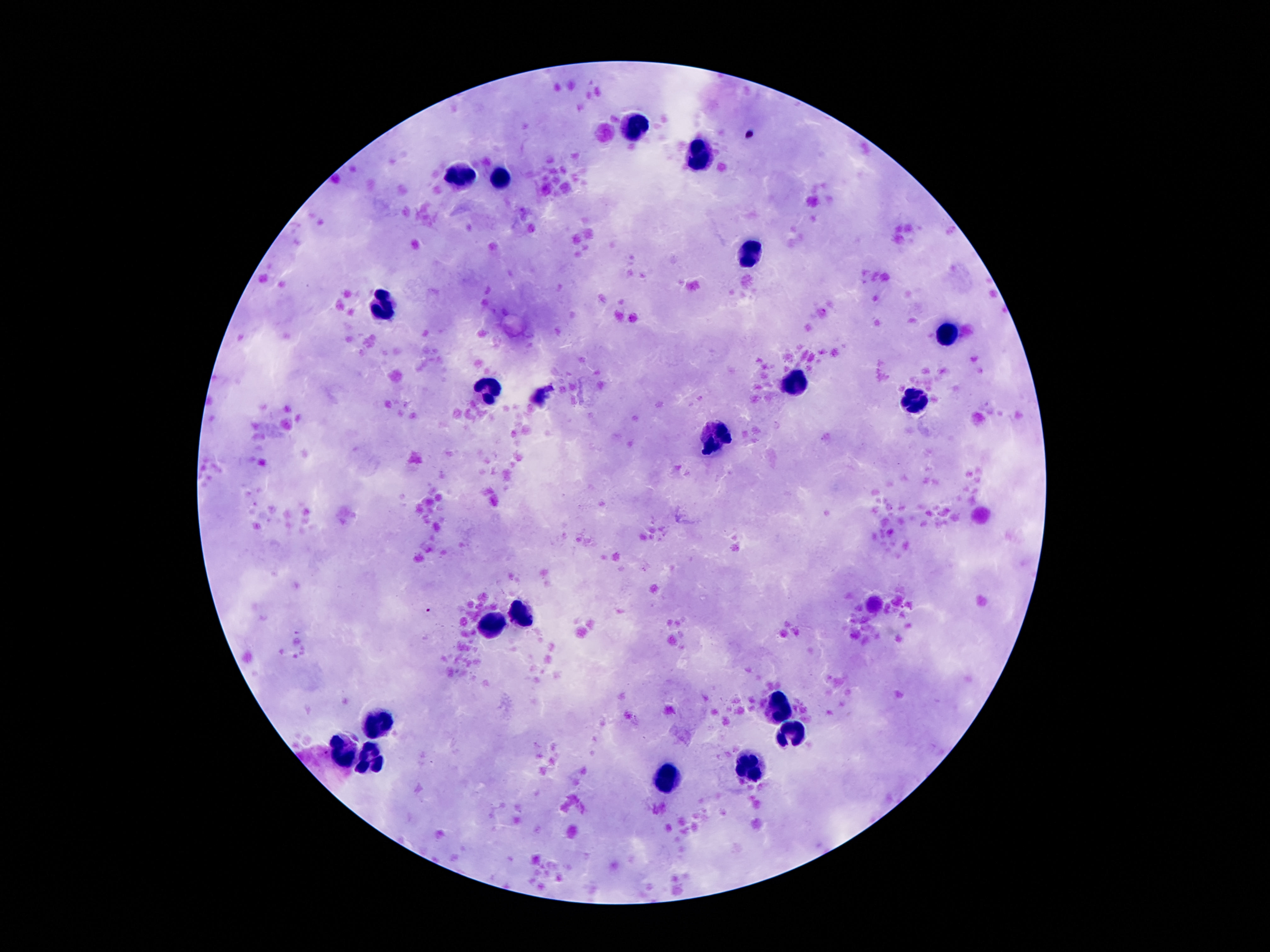
field of view = single
patient malaria status = negative
magnification = 100x
image size = 1270×952 pixels
capture = smartphone camera through the microscope eyepiece
preparation = thick blood smear
leukocyte locations = approximate object centers, in pixels from the top-left corner: (x=634, y=130), (x=701, y=158), (x=459, y=175), (x=502, y=182), (x=749, y=257), (x=387, y=310), (x=948, y=334), (x=792, y=383), (x=490, y=393), (x=915, y=403), (x=718, y=434), (x=521, y=614), (x=497, y=624), (x=775, y=707), (x=377, y=721), (x=787, y=737), (x=343, y=753), (x=372, y=765), (x=751, y=768), (x=665, y=780)
stain = Giemsa